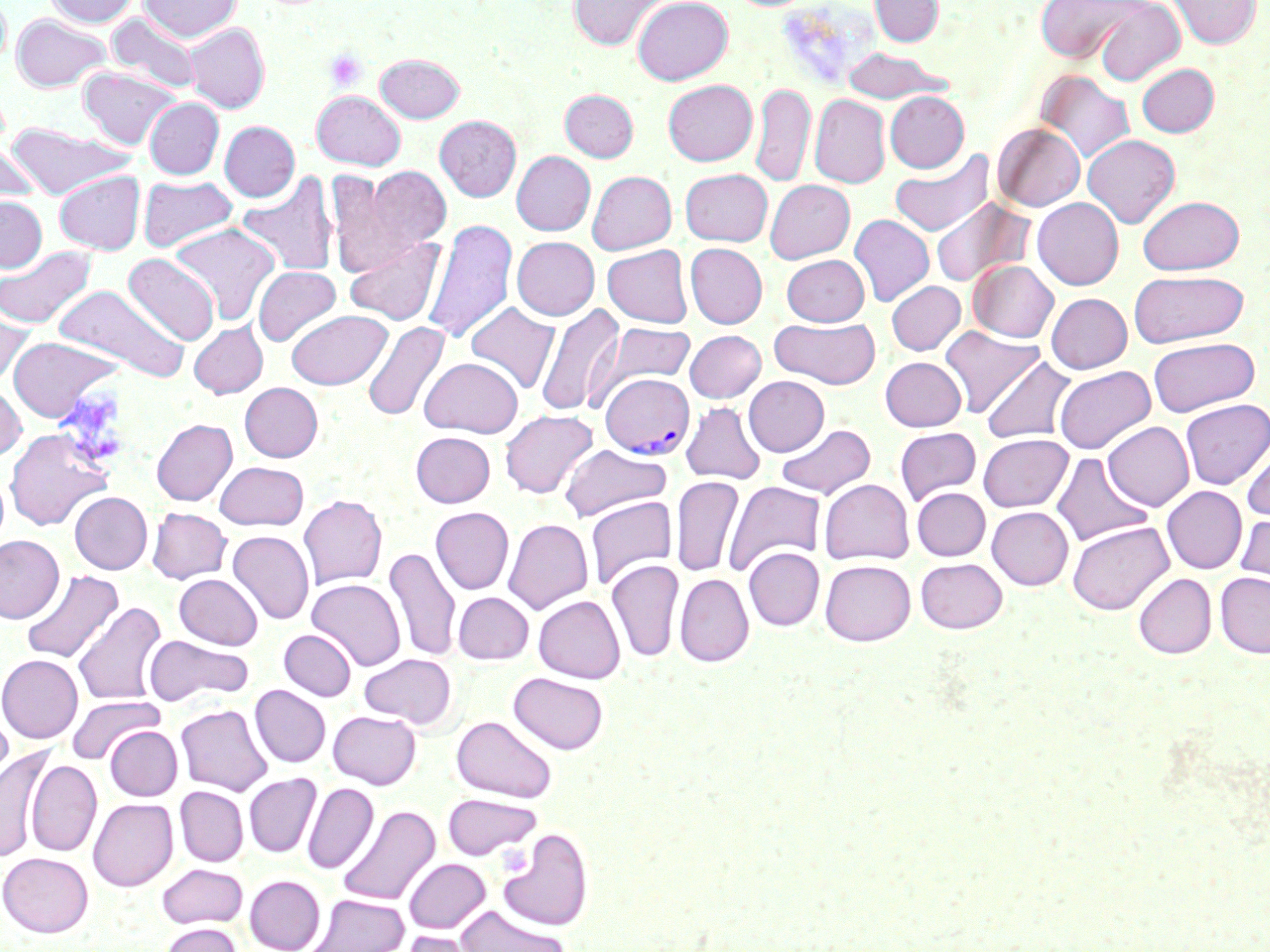 Approximate bounding boxes as named x1/y1/x2/y2 corners in pixels. Uninfected red blood cell locations: (x1=0, y1=0, x2=11, y2=69), (x1=43, y1=0, x2=140, y2=27), (x1=140, y1=0, x2=241, y2=42), (x1=567, y1=0, x2=670, y2=51), (x1=632, y1=0, x2=733, y2=85), (x1=870, y1=0, x2=944, y2=46), (x1=1033, y1=0, x2=1148, y2=63), (x1=1168, y1=0, x2=1261, y2=48), (x1=1094, y1=1, x2=1185, y2=86), (x1=11, y1=13, x2=112, y2=92), (x1=107, y1=13, x2=204, y2=94), (x1=184, y1=23, x2=270, y2=113), (x1=842, y1=47, x2=950, y2=104), (x1=375, y1=53, x2=465, y2=122), (x1=1137, y1=63, x2=1219, y2=137), (x1=78, y1=66, x2=180, y2=150), (x1=1034, y1=70, x2=1135, y2=164), (x1=663, y1=80, x2=758, y2=166), (x1=751, y1=82, x2=815, y2=188), (x1=560, y1=89, x2=638, y2=161), (x1=312, y1=91, x2=405, y2=170), (x1=884, y1=91, x2=969, y2=172), (x1=809, y1=94, x2=890, y2=188), (x1=144, y1=98, x2=224, y2=179), (x1=434, y1=115, x2=521, y2=201), (x1=219, y1=121, x2=299, y2=202), (x1=3, y1=123, x2=137, y2=199), (x1=992, y1=123, x2=1085, y2=211), (x1=1082, y1=135, x2=1180, y2=227), (x1=0, y1=143, x2=41, y2=205), (x1=889, y1=149, x2=994, y2=236), (x1=512, y1=151, x2=595, y2=235), (x1=354, y1=166, x2=453, y2=264), (x1=680, y1=168, x2=773, y2=246), (x1=54, y1=170, x2=145, y2=254), (x1=587, y1=170, x2=677, y2=255), (x1=237, y1=171, x2=339, y2=277), (x1=138, y1=176, x2=239, y2=253), (x1=765, y1=180, x2=855, y2=263), (x1=930, y1=195, x2=1035, y2=288), (x1=0, y1=196, x2=47, y2=272), (x1=1138, y1=196, x2=1244, y2=274), (x1=1032, y1=197, x2=1123, y2=289), (x1=849, y1=214, x2=934, y2=307), (x1=423, y1=220, x2=518, y2=345), (x1=169, y1=222, x2=280, y2=325), (x1=344, y1=235, x2=446, y2=326), (x1=512, y1=236, x2=599, y2=320), (x1=685, y1=243, x2=767, y2=328), (x1=602, y1=245, x2=693, y2=328), (x1=0, y1=247, x2=96, y2=330), (x1=123, y1=253, x2=220, y2=346), (x1=782, y1=254, x2=869, y2=325), (x1=969, y1=260, x2=1058, y2=342), (x1=253, y1=266, x2=341, y2=346), (x1=1129, y1=270, x2=1249, y2=347), (x1=886, y1=281, x2=966, y2=355), (x1=54, y1=283, x2=189, y2=383), (x1=1046, y1=293, x2=1132, y2=373), (x1=0, y1=302, x2=35, y2=386), (x1=465, y1=302, x2=560, y2=394), (x1=534, y1=303, x2=624, y2=417), (x1=286, y1=310, x2=391, y2=389), (x1=769, y1=317, x2=880, y2=388), (x1=363, y1=320, x2=451, y2=423), (x1=189, y1=321, x2=267, y2=398), (x1=602, y1=323, x2=694, y2=391), (x1=939, y1=325, x2=1044, y2=417), (x1=684, y1=330, x2=766, y2=403), (x1=8, y1=336, x2=123, y2=422), (x1=1148, y1=337, x2=1260, y2=416), (x1=981, y1=355, x2=1077, y2=444), (x1=880, y1=356, x2=966, y2=431), (x1=420, y1=357, x2=523, y2=437), (x1=1055, y1=365, x2=1155, y2=454), (x1=743, y1=376, x2=829, y2=456), (x1=240, y1=382, x2=322, y2=461), (x1=0, y1=383, x2=26, y2=462), (x1=1180, y1=399, x2=1270, y2=489), (x1=680, y1=401, x2=758, y2=575), (x1=681, y1=401, x2=766, y2=484), (x1=499, y1=409, x2=598, y2=498), (x1=151, y1=418, x2=237, y2=505), (x1=1103, y1=421, x2=1194, y2=511), (x1=775, y1=422, x2=875, y2=500), (x1=894, y1=427, x2=982, y2=505), (x1=5, y1=428, x2=113, y2=531), (x1=411, y1=431, x2=495, y2=507), (x1=978, y1=434, x2=1073, y2=512), (x1=1241, y1=438, x2=1270, y2=522), (x1=559, y1=444, x2=671, y2=522), (x1=1051, y1=452, x2=1153, y2=546), (x1=214, y1=461, x2=308, y2=530), (x1=671, y1=476, x2=743, y2=576), (x1=819, y1=478, x2=914, y2=565), (x1=724, y1=480, x2=826, y2=576), (x1=1162, y1=486, x2=1247, y2=573), (x1=911, y1=487, x2=990, y2=561), (x1=70, y1=492, x2=152, y2=574), (x1=298, y1=495, x2=387, y2=590), (x1=585, y1=496, x2=677, y2=590), (x1=987, y1=506, x2=1073, y2=590), (x1=147, y1=507, x2=232, y2=584), (x1=431, y1=507, x2=514, y2=594), (x1=1236, y1=513, x2=1270, y2=595), (x1=503, y1=518, x2=593, y2=614), (x1=1067, y1=521, x2=1175, y2=615), (x1=227, y1=530, x2=315, y2=625), (x1=0, y1=534, x2=64, y2=624), (x1=384, y1=546, x2=461, y2=662), (x1=743, y1=547, x2=824, y2=630), (x1=916, y1=557, x2=1007, y2=633), (x1=606, y1=559, x2=683, y2=663), (x1=820, y1=559, x2=916, y2=646), (x1=20, y1=570, x2=123, y2=665), (x1=1215, y1=572, x2=1270, y2=658), (x1=174, y1=573, x2=263, y2=649), (x1=674, y1=573, x2=754, y2=667), (x1=1133, y1=573, x2=1216, y2=658), (x1=307, y1=578, x2=406, y2=671), (x1=452, y1=591, x2=534, y2=664), (x1=533, y1=595, x2=625, y2=683), (x1=72, y1=601, x2=167, y2=707), (x1=280, y1=629, x2=356, y2=701), (x1=143, y1=634, x2=253, y2=707), (x1=359, y1=653, x2=457, y2=729), (x1=0, y1=654, x2=84, y2=743), (x1=509, y1=672, x2=608, y2=754), (x1=249, y1=685, x2=330, y2=767), (x1=66, y1=696, x2=165, y2=764), (x1=175, y1=704, x2=272, y2=796), (x1=0, y1=707, x2=14, y2=795), (x1=328, y1=709, x2=422, y2=789), (x1=452, y1=715, x2=558, y2=802), (x1=105, y1=725, x2=182, y2=800), (x1=0, y1=746, x2=55, y2=862), (x1=25, y1=760, x2=101, y2=856), (x1=244, y1=773, x2=321, y2=857), (x1=303, y1=782, x2=379, y2=874), (x1=175, y1=786, x2=248, y2=866), (x1=441, y1=793, x2=543, y2=860), (x1=88, y1=798, x2=178, y2=891), (x1=338, y1=804, x2=440, y2=907), (x1=498, y1=827, x2=592, y2=932), (x1=0, y1=852, x2=93, y2=937), (x1=404, y1=858, x2=491, y2=933), (x1=157, y1=862, x2=248, y2=929), (x1=245, y1=875, x2=325, y2=952), (x1=307, y1=893, x2=409, y2=952), (x1=457, y1=904, x2=569, y2=952), (x1=160, y1=923, x2=242, y2=952), (x1=398, y1=929, x2=483, y2=952). Plasmodium vivax-infected red blood cell locations: (x1=601, y1=372, x2=694, y2=459). Platelet locations: (x1=324, y1=47, x2=368, y2=93), (x1=497, y1=845, x2=531, y2=874). Slide-level diagnosis: Plasmodium vivax. Optical microscopy. May-Grünwald-Giemsa stain. Thin blood smear. Single field of view. Image is 1270×952 pixels. Captured at 1000x magnification.